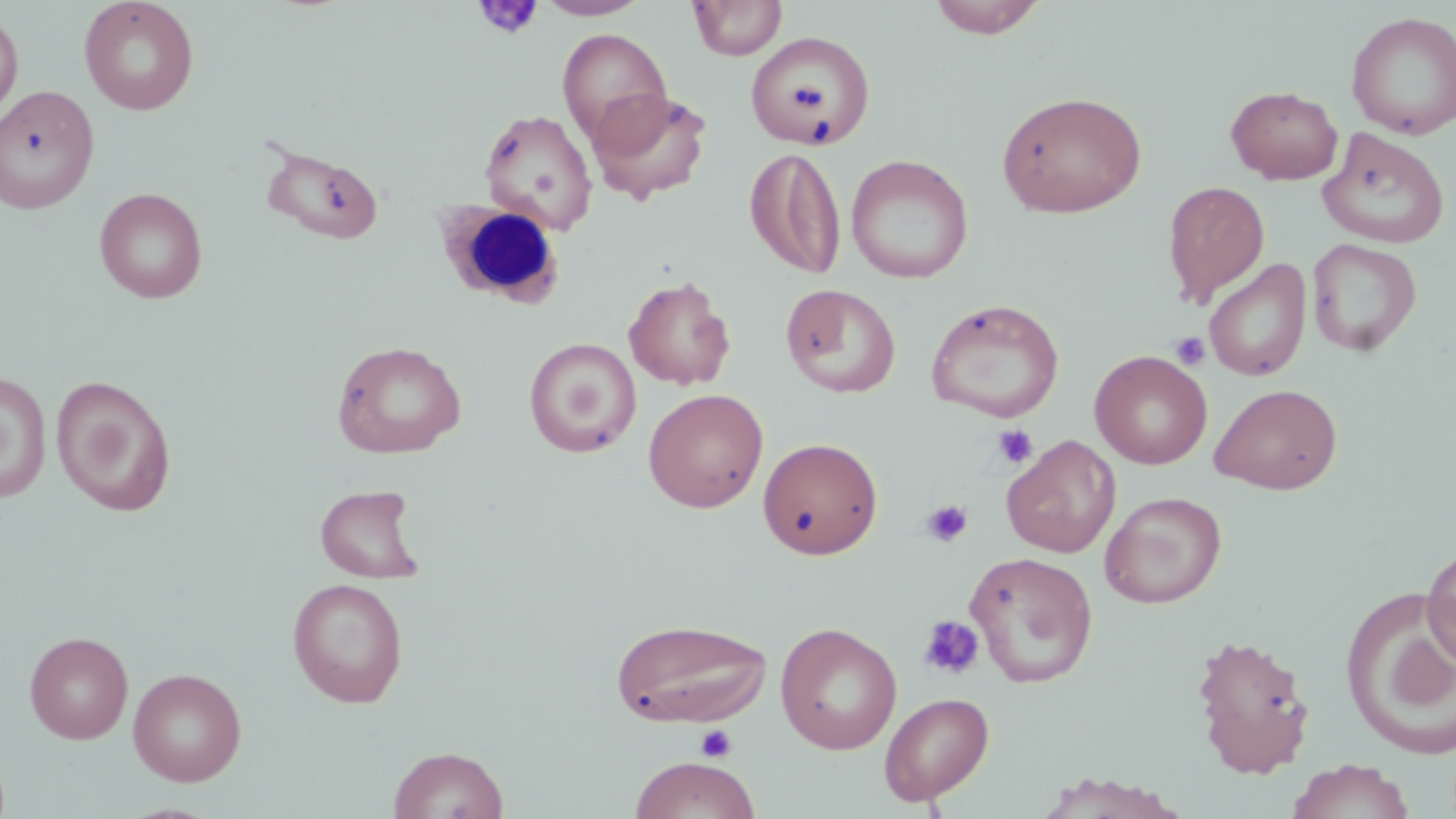

slide-level diagnosis = negative for blood parasites
magnification = 1000x
field of view = single
modality = optical microscopy
uninfected red blood cell locations = approximate bounding boxes as (x1, y1, x2, y2) in pixels: (79, 0, 199, 115), (533, 0, 651, 20), (688, 0, 787, 61), (926, 0, 1048, 39), (0, 9, 24, 121), (1345, 11, 1456, 140), (556, 28, 673, 147), (745, 31, 875, 148), (0, 85, 99, 214), (1226, 85, 1343, 184), (588, 88, 713, 207), (996, 90, 1148, 218), (478, 107, 598, 234), (1317, 129, 1451, 249), (260, 144, 387, 245), (746, 147, 846, 279), (846, 154, 973, 285), (1162, 180, 1270, 307), (94, 188, 208, 303), (1307, 238, 1422, 357), (1204, 259, 1312, 382), (623, 275, 736, 390), (780, 283, 901, 398), (925, 298, 1065, 423), (524, 337, 641, 458), (332, 340, 467, 459), (1090, 350, 1212, 469), (0, 372, 52, 503), (50, 375, 177, 515), (1209, 383, 1343, 494), (643, 388, 768, 513), (1002, 435, 1121, 558), (757, 437, 884, 560), (315, 484, 425, 584), (1100, 491, 1226, 608), (1422, 541, 1456, 674), (965, 551, 1099, 688), (287, 578, 409, 708), (1343, 593, 1456, 760), (609, 618, 773, 727), (775, 621, 903, 755), (24, 631, 134, 744), (1191, 633, 1315, 778), (128, 667, 247, 786), (879, 691, 994, 805), (388, 745, 509, 819), (629, 755, 761, 819), (1286, 759, 1416, 819), (1031, 772, 1189, 818)
stain = May-Grünwald-Giemsa
platelet locations = approximate bounding boxes as (x1, y1, x2, y2) in pixels: (475, 0, 543, 40), (1170, 331, 1210, 370), (991, 423, 1038, 470), (920, 499, 974, 548), (917, 614, 985, 680), (695, 723, 738, 763)
preparation = thin blood film
image size = 1456×819 pixels
white blood cell locations = approximate bounding boxes as (x1, y1, x2, y2) in pixels: (433, 200, 565, 308)